Identify the cell.
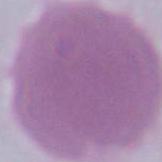

An erythrocyte.

magnification: 1000x
modality: micrograph